Classify this cell by malaria status.
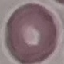

Uninfected.

Summary:
  - Stain: Giemsa
  - Image type: cell patch, automatically extracted from a larger field of view and resized to 64 × 64 pixels
  - Preparation: thin blood smear
  - Capture: smartphone through the microscope eyepiece